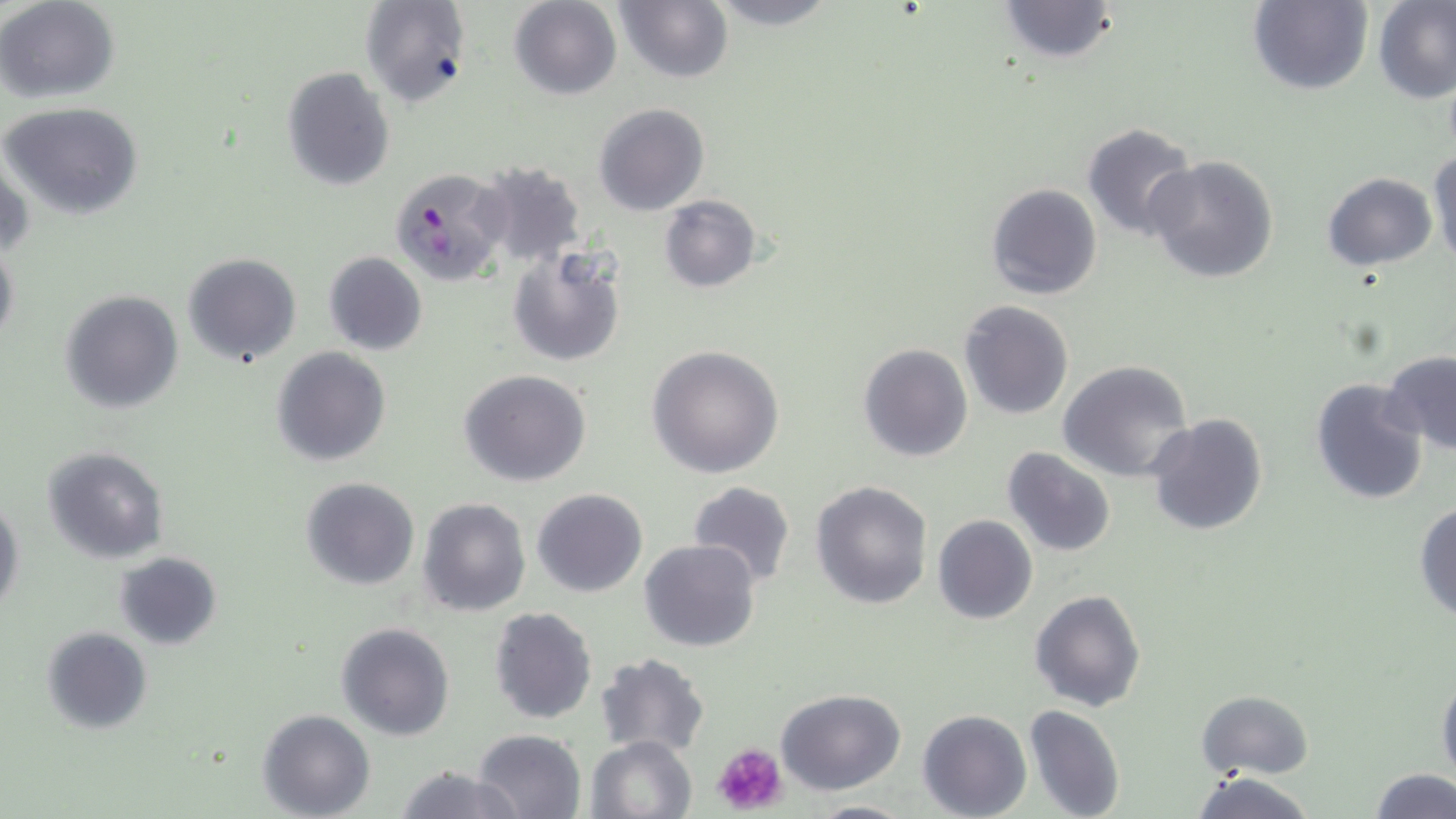 Approximate bounding boxes as (x1,y1)-(x2,y2) corner pairs in pixels. Platelet locations: (712,742)-(790,817). Uninfected red blood cell locations: (0,0)-(119,102), (358,0)-(471,109), (508,0)-(623,100), (696,0)-(848,30), (1372,0)-(1456,104), (994,1)-(1121,63), (1247,1)-(1373,96), (613,2)-(733,84), (282,67)-(394,190), (2,101)-(145,220), (593,103)-(709,216), (1081,121)-(1198,241), (1427,146)-(1456,268), (1,148)-(32,262), (1144,155)-(1279,283), (473,160)-(589,269), (1321,172)-(1436,271), (985,182)-(1103,300), (659,195)-(761,293), (0,240)-(19,349), (506,247)-(624,368), (181,252)-(303,367), (322,252)-(429,356), (59,289)-(183,414), (958,300)-(1073,420), (858,343)-(972,462), (270,345)-(392,466), (646,345)-(785,479), (1381,350)-(1456,457), (1059,361)-(1195,483), (459,369)-(592,487), (1309,378)-(1430,505), (1146,413)-(1269,536), (41,446)-(169,564), (1003,447)-(1116,558), (300,477)-(420,590), (810,480)-(932,611), (686,481)-(797,591), (533,488)-(648,597), (0,496)-(23,619), (416,497)-(531,616), (1413,501)-(1456,623), (933,515)-(1038,624), (641,539)-(762,654), (112,551)-(224,651), (1030,590)-(1146,712), (489,607)-(597,725), (336,621)-(454,740), (41,626)-(152,735), (595,652)-(710,757), (1436,670)-(1456,788), (776,687)-(907,795), (1197,689)-(1315,779), (1024,704)-(1126,819), (917,708)-(1031,819), (258,709)-(375,819), (472,728)-(586,818), (586,735)-(696,819), (392,764)-(523,819), (1368,768)-(1456,819), (1190,771)-(1320,819), (807,798)-(915,818). Plasmodium falciparum-infected red blood cell locations: (389,167)-(513,287). Slide-level diagnosis: Plasmodium falciparum. Optical microscopy. Single field of view. 1000x magnification. Thin blood film. Image is 1456×819 pixels. May-Grünwald-Giemsa stain.